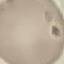
Summary:
  - Malaria status: uninfected
  - Stain: Giemsa
  - Preparation: thin smear
  - Image type: cell patch, automatically extracted from a larger field of view and resized to 64 × 64 pixels
  - Capture: smartphone camera at the microscope eyepiece